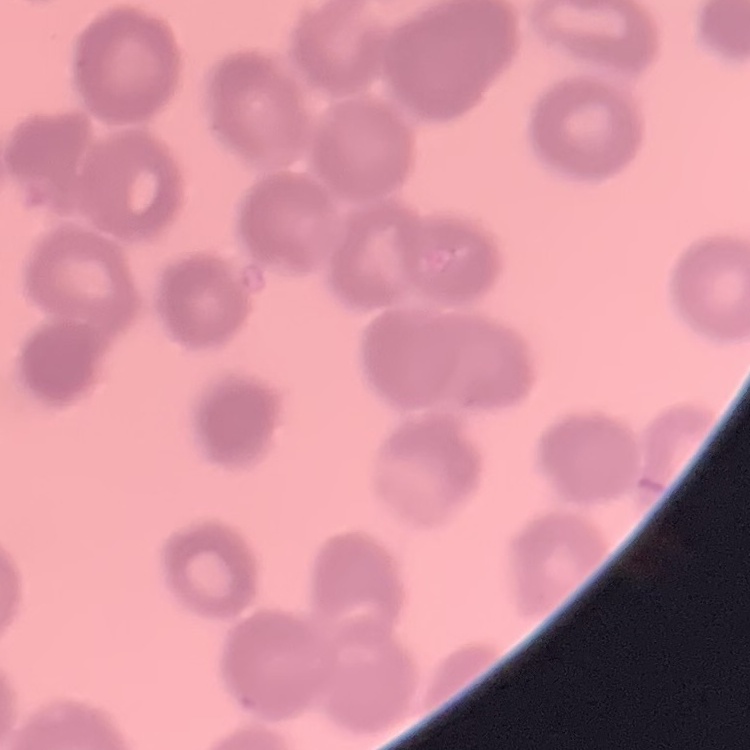

red_blood_cell_morphology: rouleaux formation
stain: Field's or Giemsa
preparation: thin blood smear
image_type: one tile cut from a larger photomicrograph